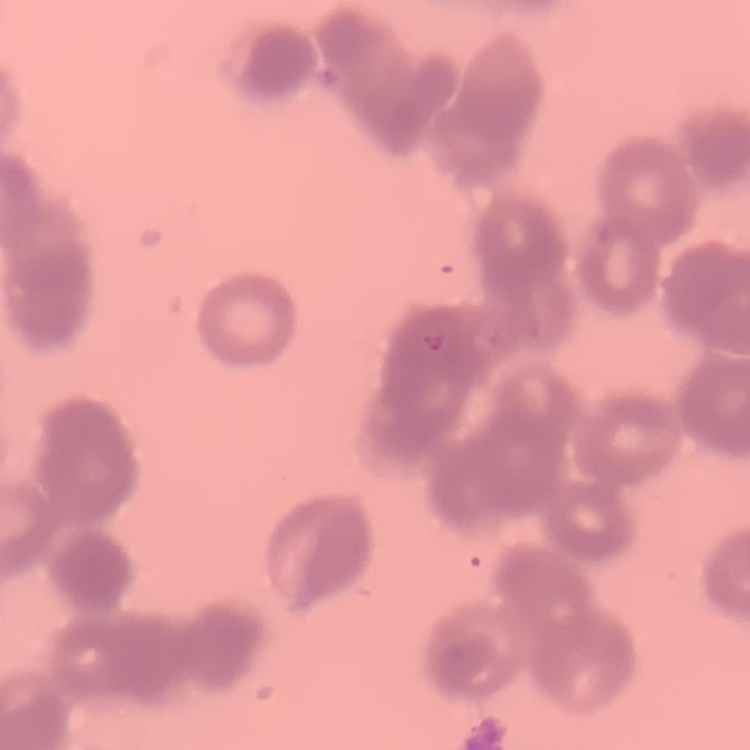

Summary:
  - Red blood cell morphology: rouleaux formation
  - Preparation: thin blood smear
  - Image type: square crop of a larger photomicrograph
  - Stain: Field's or Giemsa